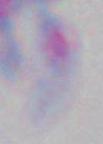 Micrograph. 1000x magnification. Toxoplasma gondii is shown.